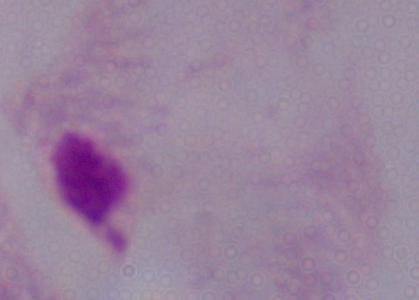

Summary:
  - Identification: trichomonad
  - Magnification: 1000x
  - Modality: micrograph